Give the position of every Plasmodium parasite.
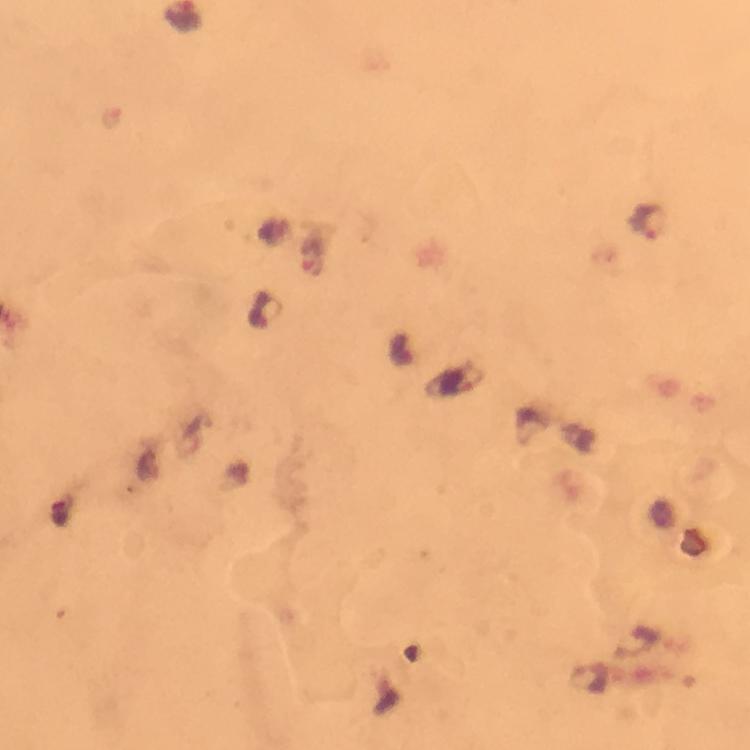
Approximate object centers, in pixels from the top-left corner.
Plasmodium parasites: (x=648, y=222), (x=314, y=251), (x=267, y=310).

Summary:
  - Magnification: 100x
  - Preparation: thick blood film
  - Capture: smartphone mounted on the microscope
  - Context: from a malaria diagnostic workup
  - Image size: 750×750 pixels
  - Immersion oil: applied
  - Stain: Giemsa
  - Cropped from: one field of view